Assess this cell for malaria.
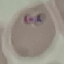

It is parasitized.

Summary:
  - Image type: automatically extracted cell patch, resized to 64 × 64 pixels
  - Preparation: thin blood film
  - Capture: smartphone through the microscope eyepiece
  - Stain: Giemsa